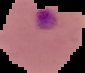
Segmented cell region on a black background. Image is 85×73 pixels. From a thin blood film. Result: Plasmodium parasites detected.